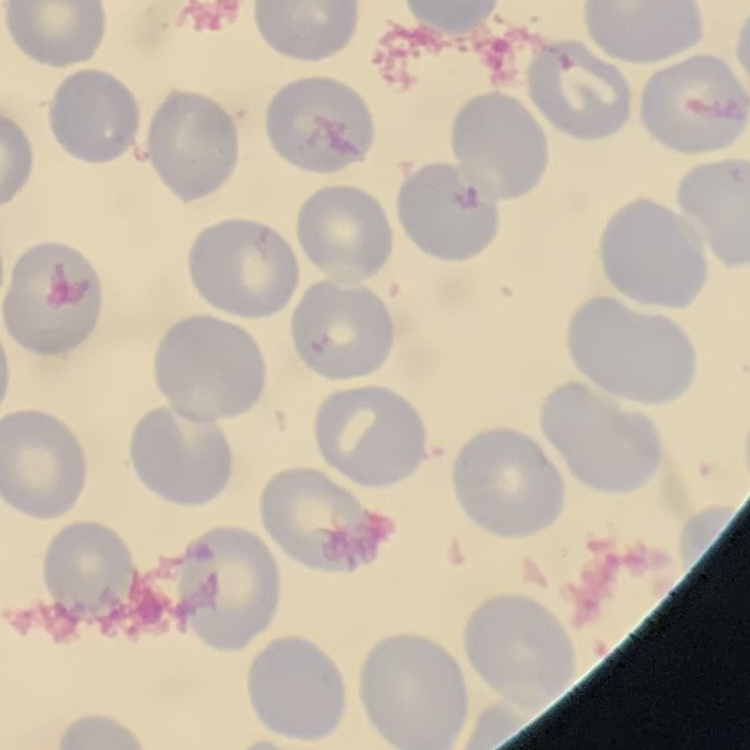
The red blood cells show no rouleaux formation. Thin peripheral smear. Square crop of a larger photomicrograph. Field's or Giemsa stain.